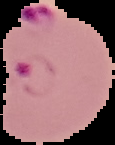

Summary:
  - Image type: cell region segmented out of the field of view; surrounding area masked to black
  - Image size: 115×145 pixels
  - Result: malaria parasites identified
  - Preparation: thin blood film